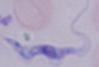
Summary:
  - Identification: trypanosome
  - Magnification: 1000x
  - Modality: micrograph